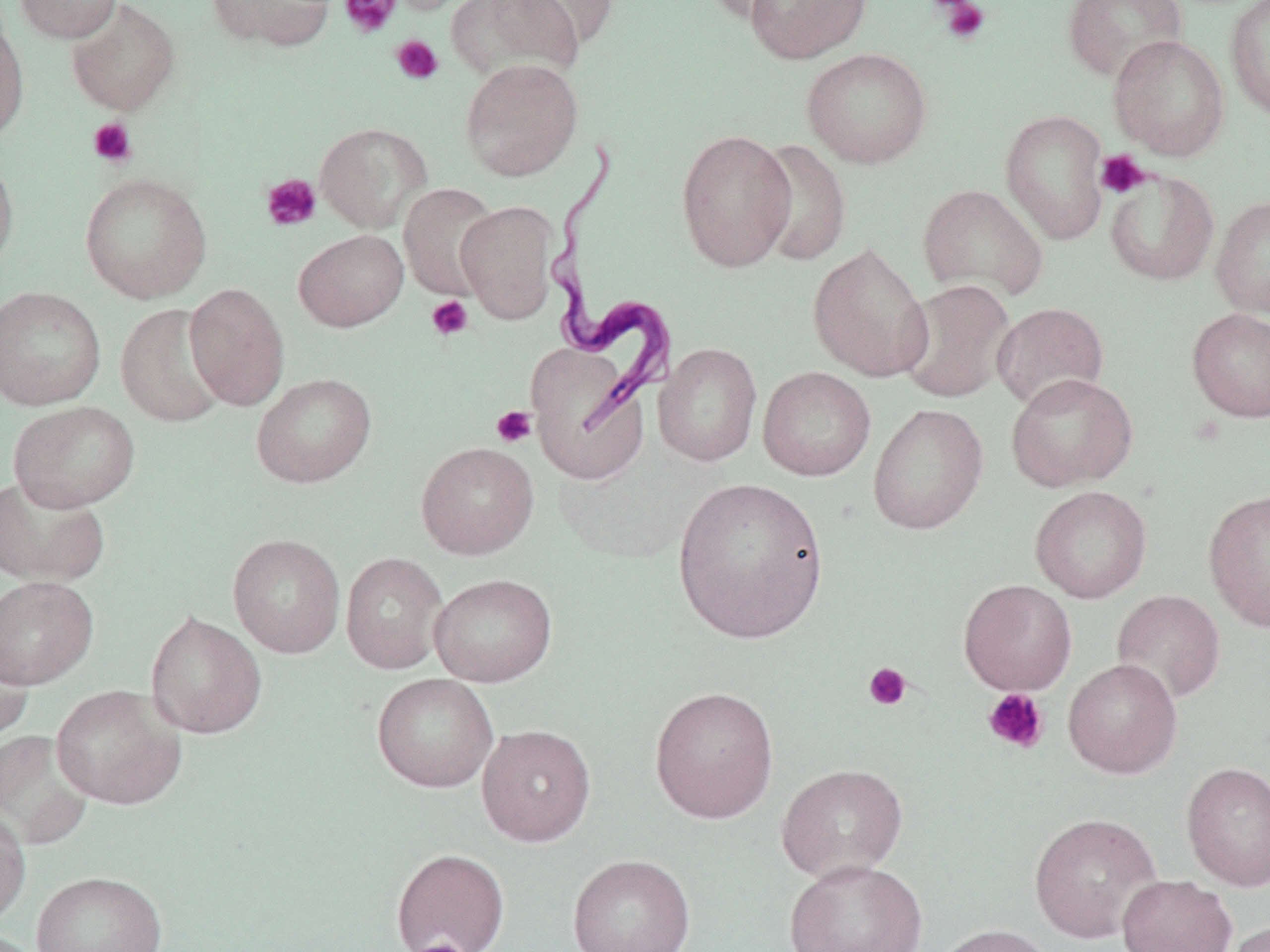
Trypanosoma brucei locations = approximate bounding boxes as [x1, y1, x2, y2] in pixels: [543, 141, 679, 438]
slide-level diagnosis = Trypanosoma brucei
preparation = thin blood smear
image size = 1270×952 pixels
stain = May-Grünwald-Giemsa
magnification = 1000x
uninfected red blood cell locations = approximate bounding boxes as [x1, y1, x2, y2] in pixels: [14, 0, 122, 43], [205, 0, 336, 51], [381, 0, 487, 16], [699, 0, 803, 23], [743, 0, 871, 64], [1062, 0, 1188, 82], [1224, 0, 1270, 121], [66, 1, 181, 116], [450, 1, 586, 82], [502, 1, 621, 52], [0, 18, 29, 144], [1108, 35, 1230, 160], [801, 47, 933, 169], [460, 58, 583, 181], [1000, 109, 1110, 245], [306, 118, 419, 333], [314, 122, 432, 232], [676, 129, 796, 273], [749, 138, 852, 267], [0, 152, 19, 275], [1104, 169, 1219, 286], [79, 172, 212, 303], [398, 183, 502, 302], [917, 184, 1047, 301], [1210, 194, 1270, 319], [456, 200, 559, 323], [293, 228, 408, 332], [807, 242, 934, 382], [898, 279, 1015, 404], [184, 283, 289, 410], [0, 286, 106, 411], [992, 302, 1109, 412], [115, 304, 230, 428], [1187, 308, 1270, 422], [526, 342, 648, 481], [654, 343, 762, 466], [758, 366, 876, 481], [251, 372, 376, 488], [1005, 372, 1138, 492], [7, 401, 141, 512], [867, 403, 988, 535], [415, 441, 539, 559], [0, 475, 110, 587], [670, 476, 830, 644], [1030, 485, 1152, 603], [1203, 488, 1270, 632], [227, 534, 345, 658], [341, 552, 448, 674], [428, 573, 557, 686], [0, 575, 98, 689], [958, 579, 1077, 695], [1112, 590, 1226, 705], [145, 611, 267, 739], [0, 637, 33, 744], [1063, 658, 1183, 778], [371, 672, 499, 793], [51, 684, 186, 810], [648, 685, 779, 823], [476, 724, 596, 846], [0, 730, 95, 852], [1181, 762, 1270, 891], [776, 763, 908, 883], [0, 808, 31, 928], [1029, 812, 1162, 943], [391, 848, 510, 952], [568, 854, 696, 952], [784, 858, 927, 952], [31, 871, 168, 952], [1117, 874, 1237, 952], [1223, 920, 1270, 952], [931, 923, 1059, 952]
field of view = one of a larger specimen
platelet locations = approximate bounding boxes as [x1, y1, x2, y2] in pixels: [340, 0, 400, 38], [934, 0, 990, 45], [390, 35, 443, 85], [87, 117, 138, 168], [1095, 150, 1150, 199], [260, 173, 322, 231], [426, 295, 474, 341], [491, 406, 537, 448], [863, 662, 912, 711], [982, 687, 1049, 754], [412, 939, 468, 951]
modality = optical microscopy